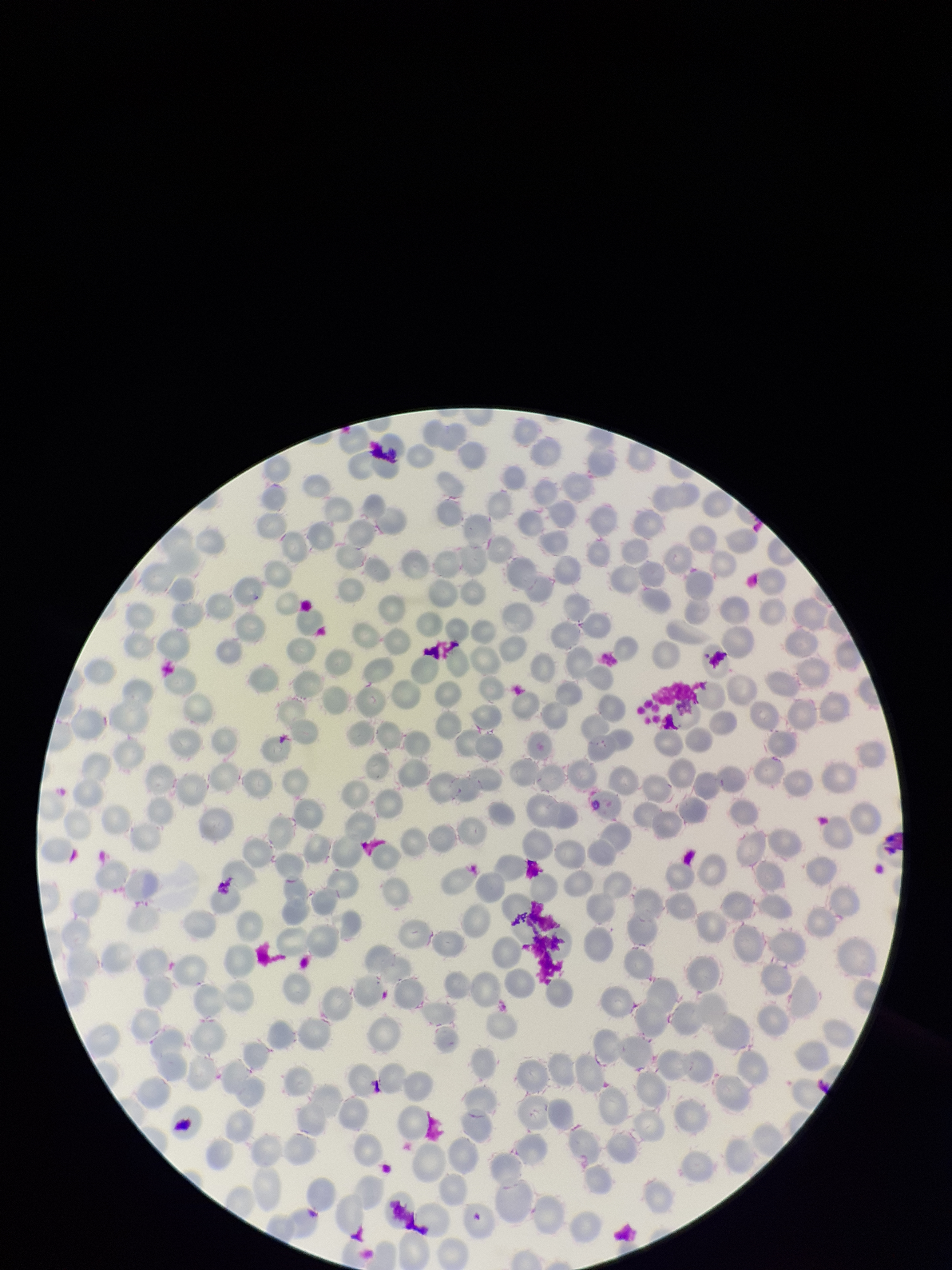
Summary:
  - Stain: Giemsa
  - Parasitized red blood cells: none seen
  - Patient malaria status: negative
  - Field of view: single
  - Image size: 952×1270 pixels
  - Red blood cell count: 290
  - Capture: smartphone photograph through the microscope eyepiece
  - Parasitized red blood cell count: 0
  - Preparation: thin